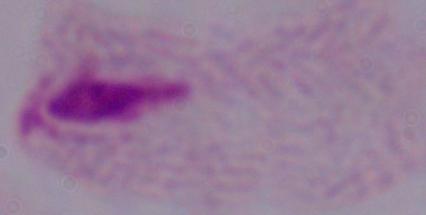 Micrograph. A trichomonad is shown. 1000x magnification.